Describe the morphology of the erythrocytes.
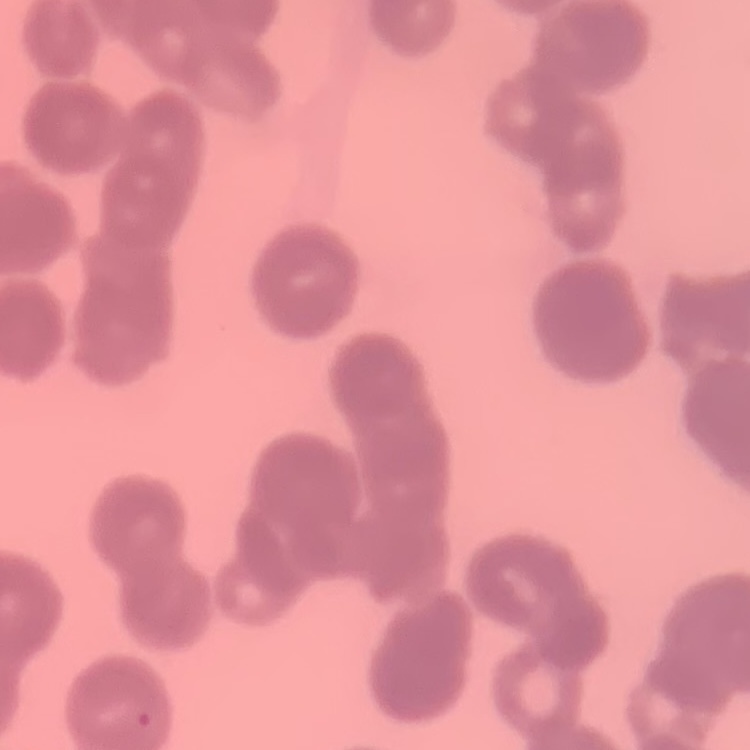

They show rouleaux formation.

Summary:
  - Image type: one tile cut from a larger photomicrograph
  - Preparation: thin blood film
  - Stain: Field's or Giemsa